Assess this cell for malaria.
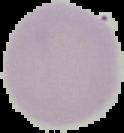
It is uninfected.

Summary:
  - Preparation: thin blood smear
  - Image type: segmented cell region on a black background
  - Image size: 124×133 pixels